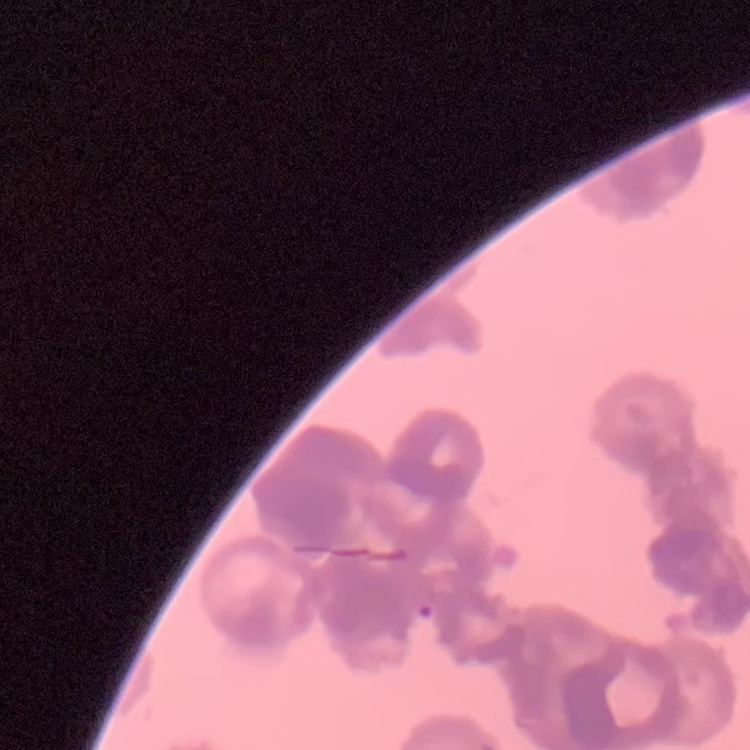
Summary:
  - Red blood cell morphology: rouleaux formation
  - Image type: one tile cut from a larger photomicrograph
  - Stain: Field's or Giemsa
  - Preparation: thin peripheral smear